Comment on the morphology of the erythrocytes.
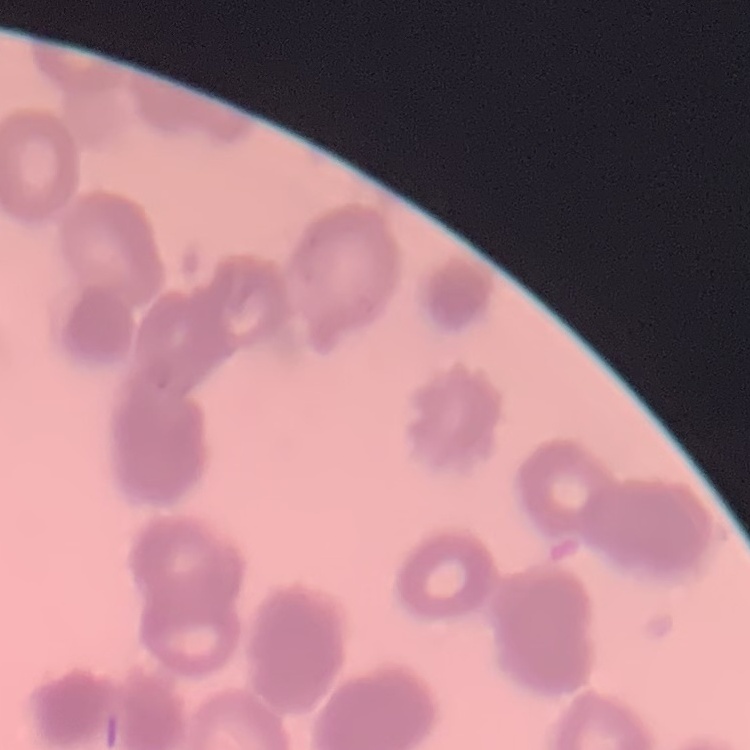
They show rouleaux formation.

Summary:
  - Stain: Field's or Giemsa
  - Preparation: thin peripheral smear
  - Image type: one tile cut from a larger photomicrograph